Classify this cell by malaria status.
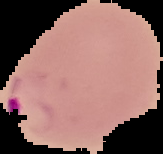
It is parasitized.

{
  "image_size": "163×154 pixels",
  "preparation": "thin blood film",
  "image_type": "segmented cell region with the area outside set to black"
}